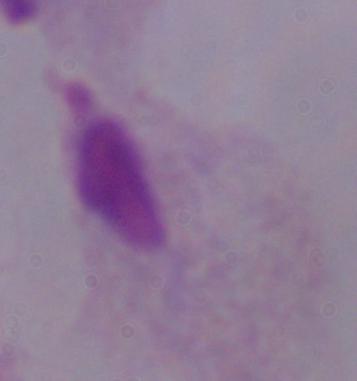
Summary:
  - Identification: trichomonad
  - Magnification: 1000x
  - Modality: photomicrograph